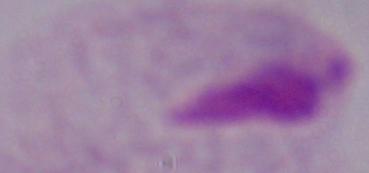
Summary:
  - Magnification: 1000x
  - Modality: photomicrograph
  - Identification: trichomonad